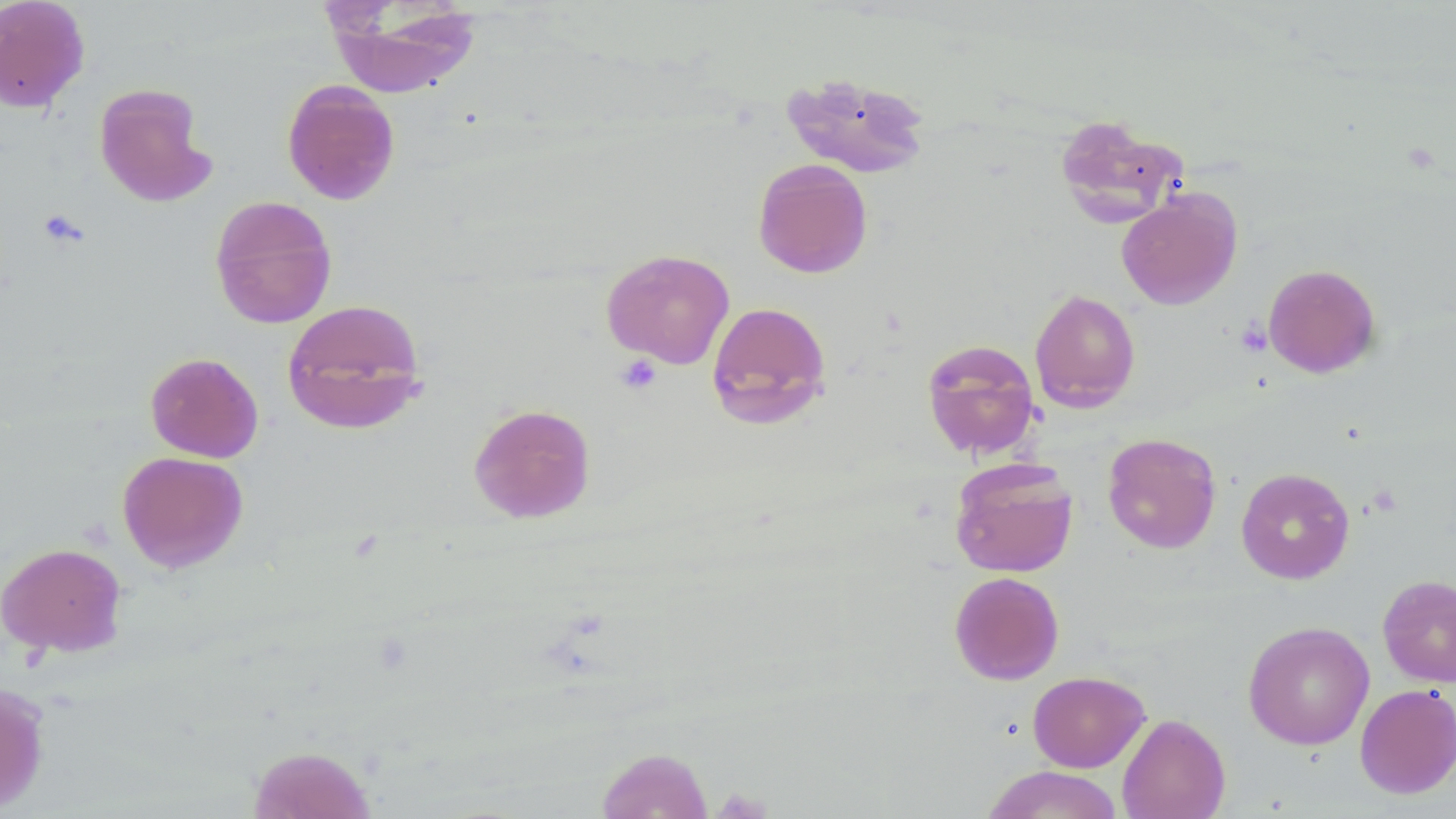

Approximate bounding boxes as (x1,y1)-(x2,y2) corner pairs in pixels. Uninfected red blood cell locations: (0,0)-(90,113), (323,2)-(481,99), (781,72)-(933,179), (282,80)-(400,205), (93,83)-(216,206), (1053,115)-(1188,230), (753,159)-(873,279), (1116,189)-(1242,310), (209,195)-(338,329), (601,248)-(736,369), (1262,263)-(1381,378), (1029,289)-(1141,413), (282,298)-(428,435), (706,301)-(832,430), (921,339)-(1040,459), (145,352)-(264,462), (469,403)-(596,523), (1102,433)-(1221,553), (117,451)-(248,572), (949,457)-(1079,578), (1235,466)-(1355,584), (0,542)-(127,657), (949,570)-(1065,685), (1377,574)-(1456,688), (1243,620)-(1374,750), (1027,670)-(1150,772), (0,682)-(50,814), (1355,683)-(1456,798), (1117,713)-(1230,819), (248,745)-(376,819), (596,747)-(713,818), (982,765)-(1125,819). Platelet locations: (1236,319)-(1272,356), (616,355)-(661,395). Slide-level diagnosis: no evidence of blood parasites. Image is 1456×819 pixels. Thin blood smear. Light microscopy. 1000x magnification. May-Grünwald-Giemsa-stained preparation. Single field of view.